Evaluate for Plasmodium parasites.
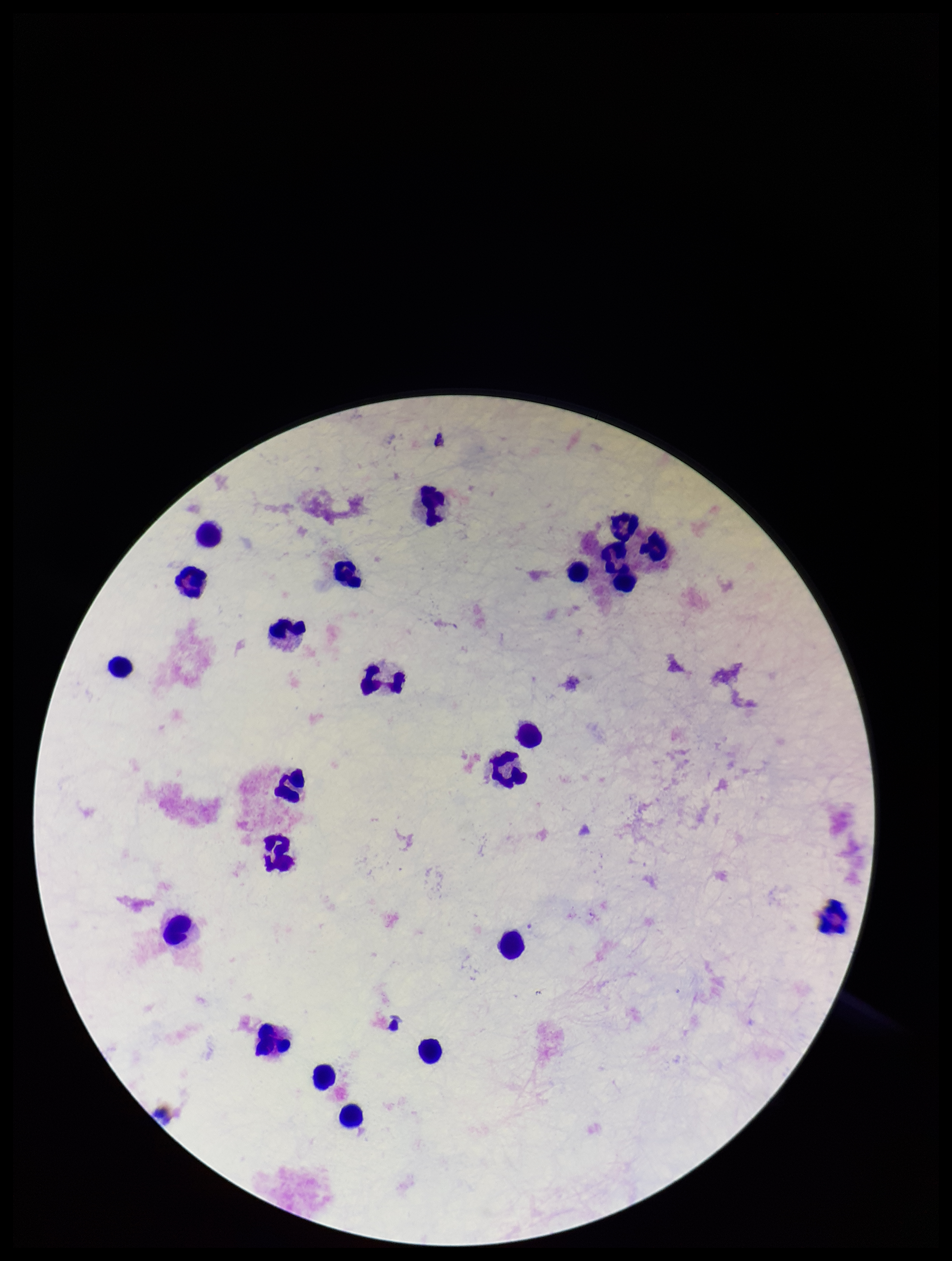

None seen.

image size = 952×1261 pixels
leukocyte count = 22
capture = smartphone photograph through the microscope eyepiece
parasite count = 0
patient malaria status = negative
field of view = single
preparation = thick smear
stain = Giemsa